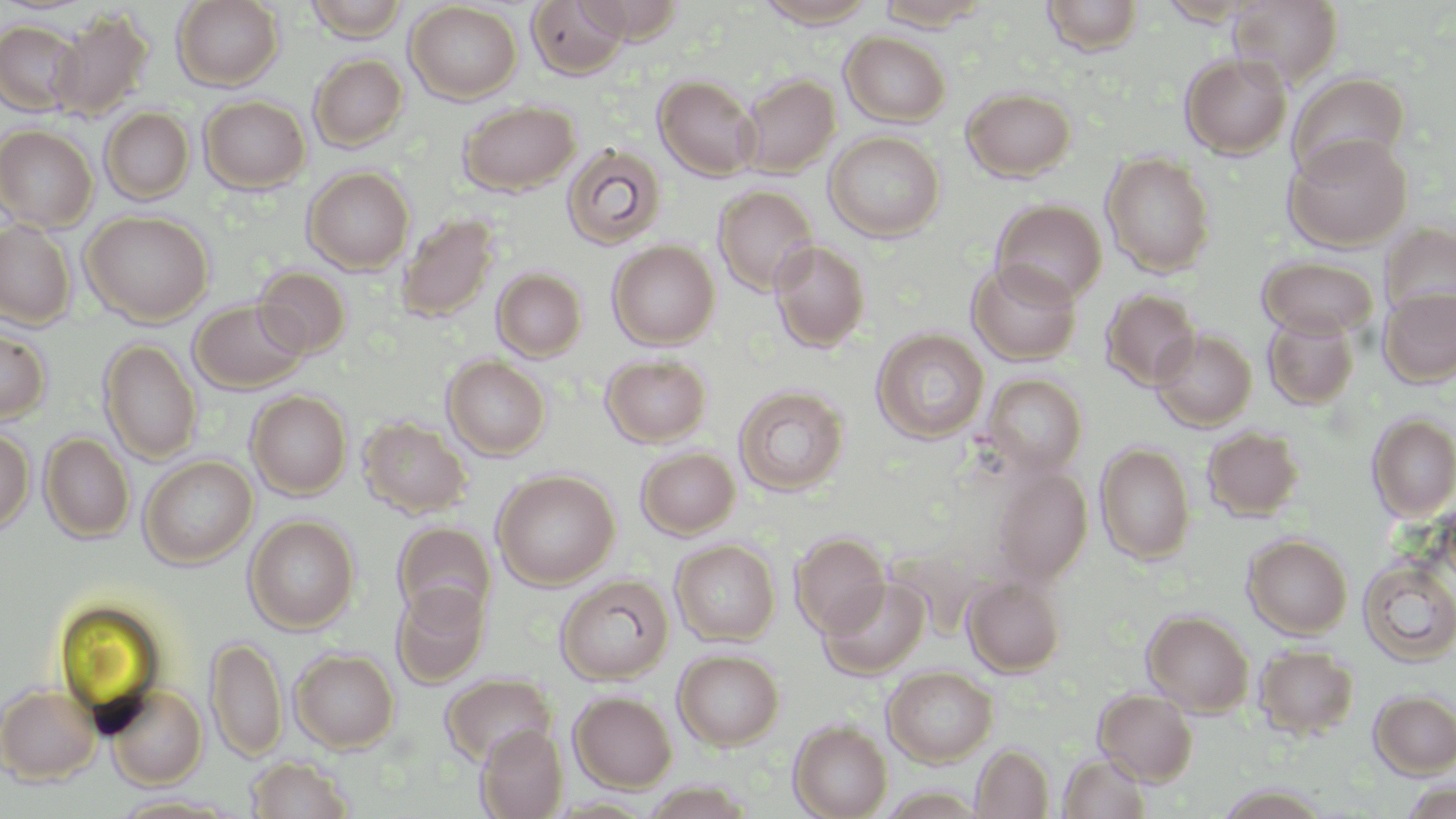 Approximate bounding boxes as (x1, y1, x2, y2) in pixels. Uninfected red blood cell locations: (172, 0, 284, 90), (305, 0, 409, 41), (527, 0, 630, 79), (576, 0, 687, 42), (754, 0, 880, 28), (1041, 0, 1144, 55), (1155, 0, 1265, 26), (1228, 0, 1343, 86), (872, 1, 992, 29), (405, 2, 522, 103), (48, 10, 153, 121), (0, 20, 84, 116), (840, 31, 951, 127), (1180, 53, 1292, 159), (309, 54, 408, 151), (1287, 72, 1411, 181), (738, 74, 840, 178), (654, 75, 760, 180), (962, 87, 1076, 182), (199, 96, 310, 193), (457, 100, 580, 196), (100, 107, 195, 204), (0, 124, 97, 231), (824, 131, 945, 242), (1284, 133, 1413, 251), (561, 144, 667, 251), (1102, 151, 1216, 277), (303, 166, 414, 273), (713, 185, 819, 296), (992, 199, 1108, 305), (81, 211, 213, 325), (395, 213, 500, 323), (0, 220, 76, 329), (1381, 223, 1456, 322), (769, 239, 870, 353), (608, 240, 720, 349), (1258, 257, 1379, 339), (967, 260, 1082, 365), (254, 265, 352, 358), (492, 268, 587, 361), (1379, 287, 1456, 388), (1101, 288, 1201, 391), (190, 299, 310, 393), (1262, 311, 1360, 410), (0, 325, 50, 425), (1152, 328, 1257, 431), (872, 329, 989, 444), (99, 338, 202, 464), (600, 354, 712, 447), (443, 355, 550, 459), (982, 374, 1087, 477), (734, 385, 849, 496), (247, 390, 351, 499), (1368, 413, 1456, 520), (358, 417, 472, 519), (1202, 427, 1304, 521), (0, 428, 34, 534), (40, 433, 134, 543), (1096, 443, 1196, 564), (635, 447, 740, 539), (139, 455, 257, 569), (991, 466, 1092, 584), (492, 469, 619, 589), (1438, 493, 1456, 591), (244, 515, 359, 633), (392, 521, 496, 625), (790, 532, 890, 636), (1243, 534, 1353, 638), (670, 539, 780, 646), (1358, 559, 1456, 666), (555, 575, 674, 685), (963, 575, 1066, 676), (821, 576, 930, 677), (392, 582, 490, 687), (1142, 610, 1255, 715), (206, 635, 287, 762), (1253, 644, 1360, 738), (291, 649, 399, 752), (673, 649, 784, 750), (883, 666, 998, 767), (441, 673, 557, 768), (0, 684, 101, 784), (105, 685, 207, 789), (1095, 688, 1198, 784), (1370, 690, 1456, 777), (569, 691, 677, 792), (789, 720, 893, 819), (476, 725, 568, 819), (972, 744, 1054, 818), (1059, 752, 1152, 818), (247, 756, 354, 818), (1401, 781, 1455, 819), (1214, 785, 1333, 818), (111, 794, 239, 817). Slide-level diagnosis: no evidence of blood parasites. May-Grünwald-Giemsa-stained preparation. Thin blood film. Image is 1456×819 pixels. Single field of view. Optical microscopy. Captured at 1000x magnification.